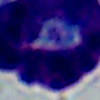
identification: leukocyte
magnification: 1000x
modality: photomicrograph